Give the extent of all Plasmodium malariae-infected red blood cells.
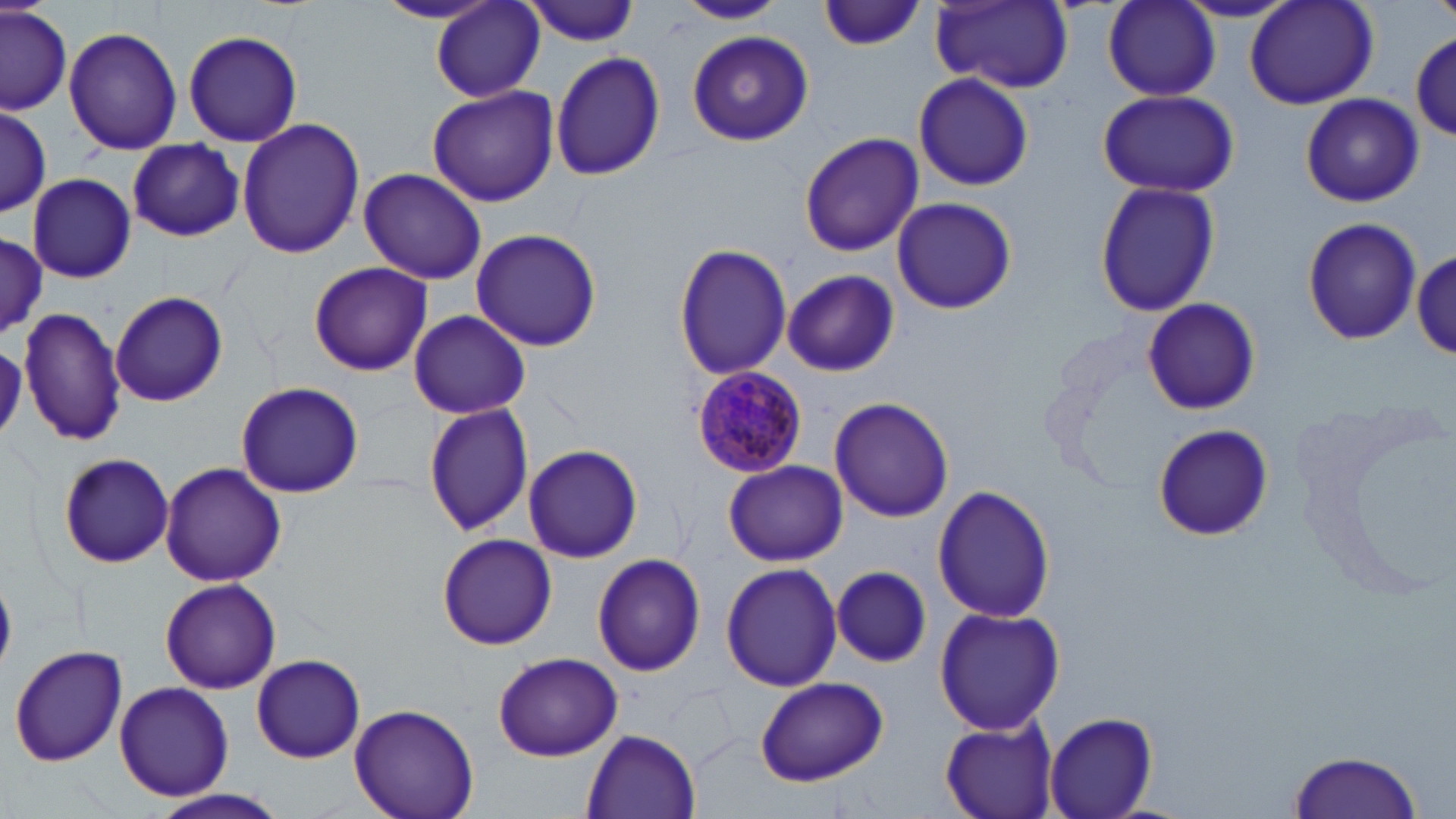

Approximate bounding boxes as (x1,y1)-(x2,y2) corner pairs in pixels.
Plasmodium malariae-infected red blood cells: (690,363)-(810,476).

slide_level_diagnosis: Plasmodium malariae
preparation: thin blood film
modality: optical microscopy
field_of_view: single
magnification: 1000x
image_size: 1456×819 pixels
uninfected_red_blood_cell_locations: 'approximate bounding boxes as (x1,y1)-(x2,y2) corner pairs in pixels: (677,0)-(786,24), (929,0)-(1074,91), (1175,0)-(1302,22), (1244,0)-(1381,110), (371,1)-(501,24), (431,1)-(547,102), (522,1)-(644,46), (819,1)-(925,51), (1102,1)-(1220,102), (1,4)-(72,116), (63,25)-(182,155), (687,28)-(813,146), (183,29)-(303,148), (1411,36)-(1456,143), (550,51)-(665,181), (913,71)-(1033,193), (426,85)-(558,208), (1097,88)-(1239,198), (1300,92)-(1424,207), (0,106)-(51,220), (236,117)-(366,259), (799,133)-(923,256), (124,140)-(249,242), (358,170)-(485,283), (26,172)-(136,283), (1093,179)-(1220,319), (890,196)-(1018,315), (1301,216)-(1422,345), (470,227)-(605,353), (0,235)-(47,336), (673,241)-(793,379), (1411,250)-(1456,362), (307,262)-(433,377), (782,269)-(899,377), (111,290)-(228,406), (1141,297)-(1261,415), (20,304)-(128,446), (408,309)-(530,419), (235,381)-(364,498), (829,396)-(954,522), (1293,400)-(1453,602), (423,401)-(535,539), (1150,424)-(1273,542), (523,443)-(644,564), (57,451)-(175,568), (722,460)-(847,566), (159,463)-(288,585), (932,484)-(1058,624), (437,534)-(556,650), (592,553)-(706,677), (721,563)-(842,691), (831,566)-(932,667), (159,578)-(283,694), (935,606)-(1065,736), (9,644)-(129,768), (491,652)-(623,762), (251,653)-(366,764), (754,677)-(888,786), (115,683)-(232,799), (350,704)-(477,819), (1042,711)-(1157,819), (939,716)-(1061,819), (583,729)-(701,817), (1287,748)-(1425,819), (145,789)-(291,819)'
stain: May-Grünwald-Giemsa